Assess the morphology of the erythrocytes.
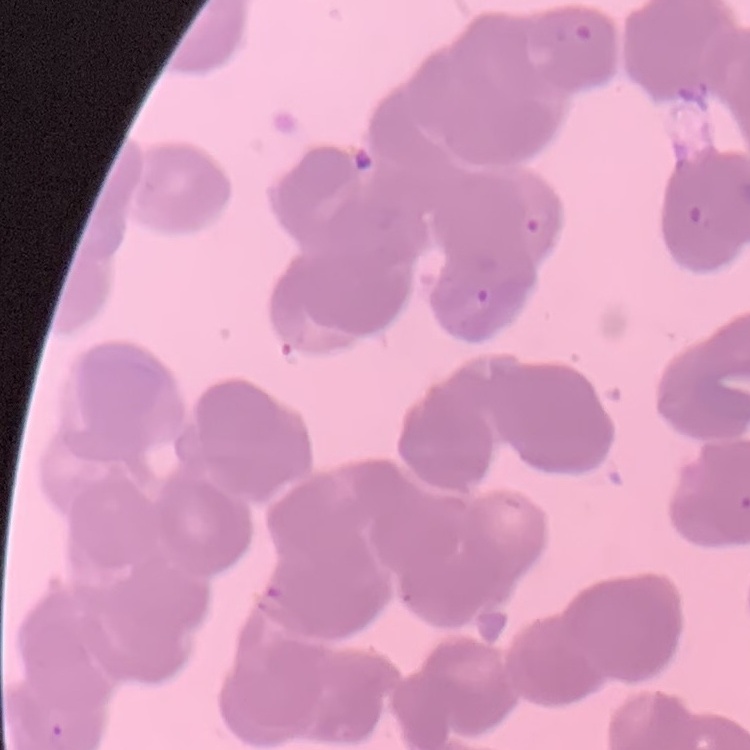
Rouleaux formation.

One tile cut from a larger photomicrograph. Stained with either Field's or Giemsa. Thin blood film.